Outline each blood parasite and name the species.
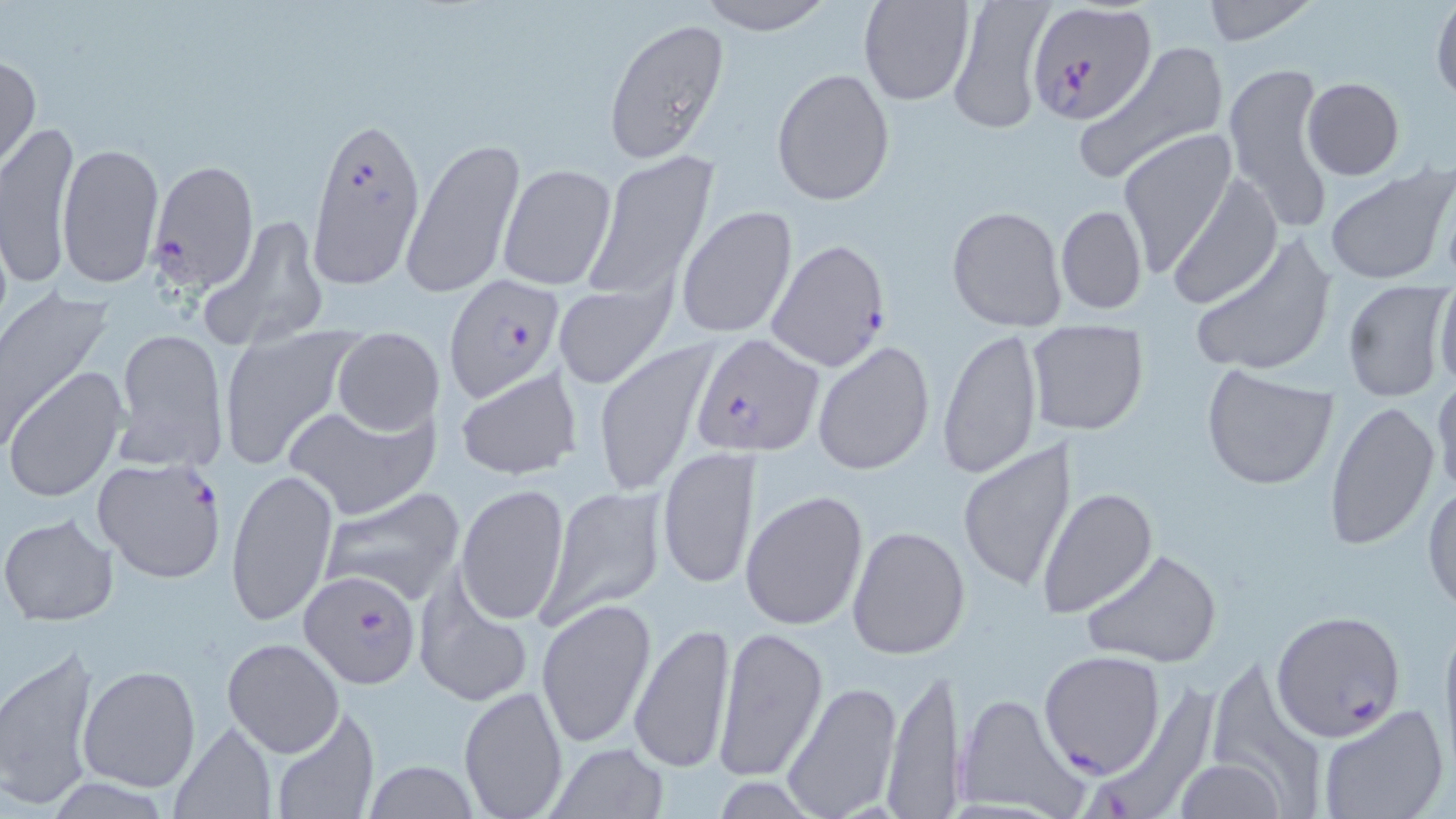
Approximate bounding boxes as named x1/y1/x2/y2 corners in pixels.
Plasmodium falciparum-infected red blood cells: (x1=1028, y1=2, x2=1157, y2=123), (x1=306, y1=112, x2=427, y2=289), (x1=149, y1=160, x2=259, y2=290), (x1=767, y1=238, x2=890, y2=371), (x1=446, y1=276, x2=563, y2=402), (x1=690, y1=333, x2=822, y2=458), (x1=91, y1=456, x2=225, y2=583), (x1=300, y1=569, x2=422, y2=690), (x1=1270, y1=610, x2=1407, y2=741), (x1=1038, y1=649, x2=1166, y2=777), (x1=1086, y1=680, x2=1219, y2=819).
No Plasmodium ovale, Plasmodium malariae, Plasmodium vivax, Babesia divergens, or Trypanosoma brucei observed.

slide_level_diagnosis: Plasmodium falciparum
uninfected_red_blood_cell_locations: 'approximate bounding boxes as named x1/y1/x2/y2 corners in pixels: (x1=694, y1=0, x2=836, y2=36), (x1=859, y1=0, x2=975, y2=106), (x1=1199, y1=0, x2=1318, y2=48), (x1=1429, y1=0, x2=1456, y2=106), (x1=946, y1=1, x2=1053, y2=136), (x1=602, y1=17, x2=730, y2=163), (x1=1074, y1=43, x2=1231, y2=187), (x1=1, y1=52, x2=41, y2=173), (x1=1223, y1=61, x2=1338, y2=233), (x1=771, y1=67, x2=895, y2=206), (x1=1301, y1=77, x2=1404, y2=181), (x1=1, y1=120, x2=79, y2=284), (x1=1117, y1=130, x2=1235, y2=276), (x1=405, y1=136, x2=525, y2=302), (x1=55, y1=141, x2=165, y2=288), (x1=585, y1=153, x2=720, y2=299), (x1=497, y1=162, x2=618, y2=290), (x1=1324, y1=168, x2=1453, y2=284), (x1=1167, y1=171, x2=1281, y2=310), (x1=675, y1=204, x2=798, y2=340), (x1=1056, y1=204, x2=1148, y2=315), (x1=947, y1=205, x2=1067, y2=330), (x1=200, y1=214, x2=329, y2=352), (x1=1189, y1=230, x2=1337, y2=379), (x1=1434, y1=276, x2=1456, y2=391), (x1=1341, y1=279, x2=1450, y2=402), (x1=554, y1=285, x2=672, y2=389), (x1=0, y1=288, x2=112, y2=449), (x1=1025, y1=320, x2=1149, y2=435), (x1=216, y1=325, x2=357, y2=469), (x1=938, y1=325, x2=1043, y2=480), (x1=112, y1=326, x2=229, y2=474), (x1=332, y1=327, x2=444, y2=437), (x1=593, y1=339, x2=719, y2=496), (x1=811, y1=341, x2=935, y2=475), (x1=1199, y1=365, x2=1340, y2=492), (x1=454, y1=367, x2=581, y2=481), (x1=5, y1=368, x2=125, y2=502), (x1=1431, y1=377, x2=1455, y2=500), (x1=1324, y1=399, x2=1438, y2=551), (x1=284, y1=402, x2=439, y2=521), (x1=957, y1=440, x2=1079, y2=593), (x1=657, y1=445, x2=761, y2=590), (x1=226, y1=466, x2=337, y2=627), (x1=454, y1=482, x2=570, y2=625), (x1=540, y1=483, x2=668, y2=625), (x1=1424, y1=483, x2=1456, y2=615), (x1=316, y1=484, x2=466, y2=607), (x1=1036, y1=487, x2=1158, y2=618), (x1=740, y1=489, x2=870, y2=632), (x1=0, y1=512, x2=119, y2=626), (x1=847, y1=524, x2=970, y2=661), (x1=1083, y1=548, x2=1221, y2=670), (x1=413, y1=577, x2=534, y2=710), (x1=535, y1=598, x2=656, y2=750), (x1=1438, y1=612, x2=1456, y2=773), (x1=628, y1=622, x2=736, y2=774), (x1=712, y1=628, x2=828, y2=784), (x1=223, y1=639, x2=344, y2=756), (x1=0, y1=644, x2=102, y2=811), (x1=1219, y1=661, x2=1326, y2=819), (x1=78, y1=664, x2=201, y2=793), (x1=882, y1=665, x2=962, y2=819), (x1=778, y1=681, x2=902, y2=819), (x1=457, y1=684, x2=570, y2=818), (x1=951, y1=688, x2=1091, y2=818), (x1=1316, y1=704, x2=1449, y2=819), (x1=265, y1=707, x2=379, y2=819), (x1=167, y1=720, x2=277, y2=818), (x1=543, y1=740, x2=669, y2=818), (x1=363, y1=759, x2=479, y2=819), (x1=1172, y1=759, x2=1289, y2=817)'
preparation: thin blood film
field_of_view: single
magnification: 1000x
stain: May-Grünwald-Giemsa
image_size: 1456×819 pixels
modality: optical microscopy